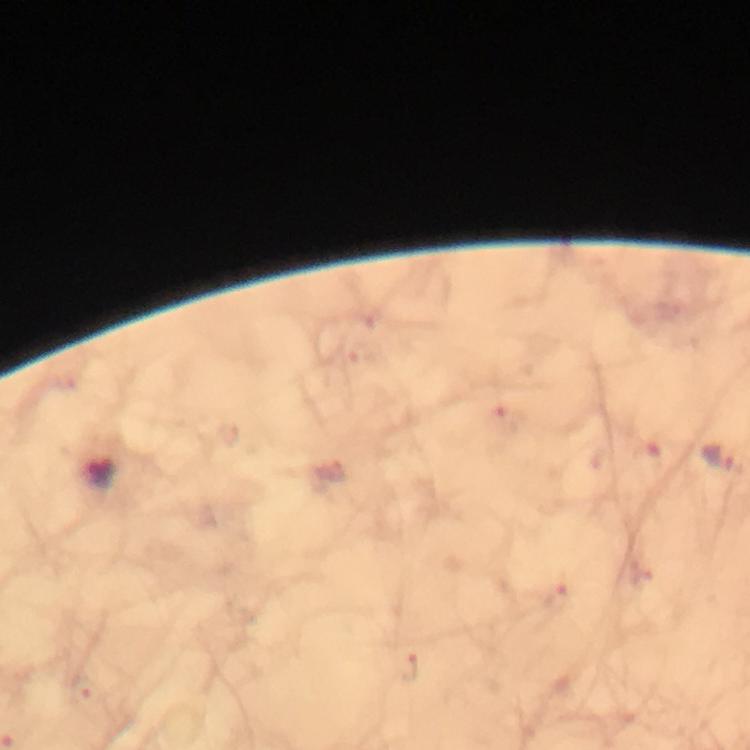 Approximate centers as (x, y) in pixels. Malaria parasite locations: (718, 458). Giemsa-stained preparation. A crop from one field of view. Photographed with a smartphone mounted on the microscope. From a malaria diagnostic workup. Immersion oil was used. At 100x magnification. Thick blood film. Image is 750×750 pixels.